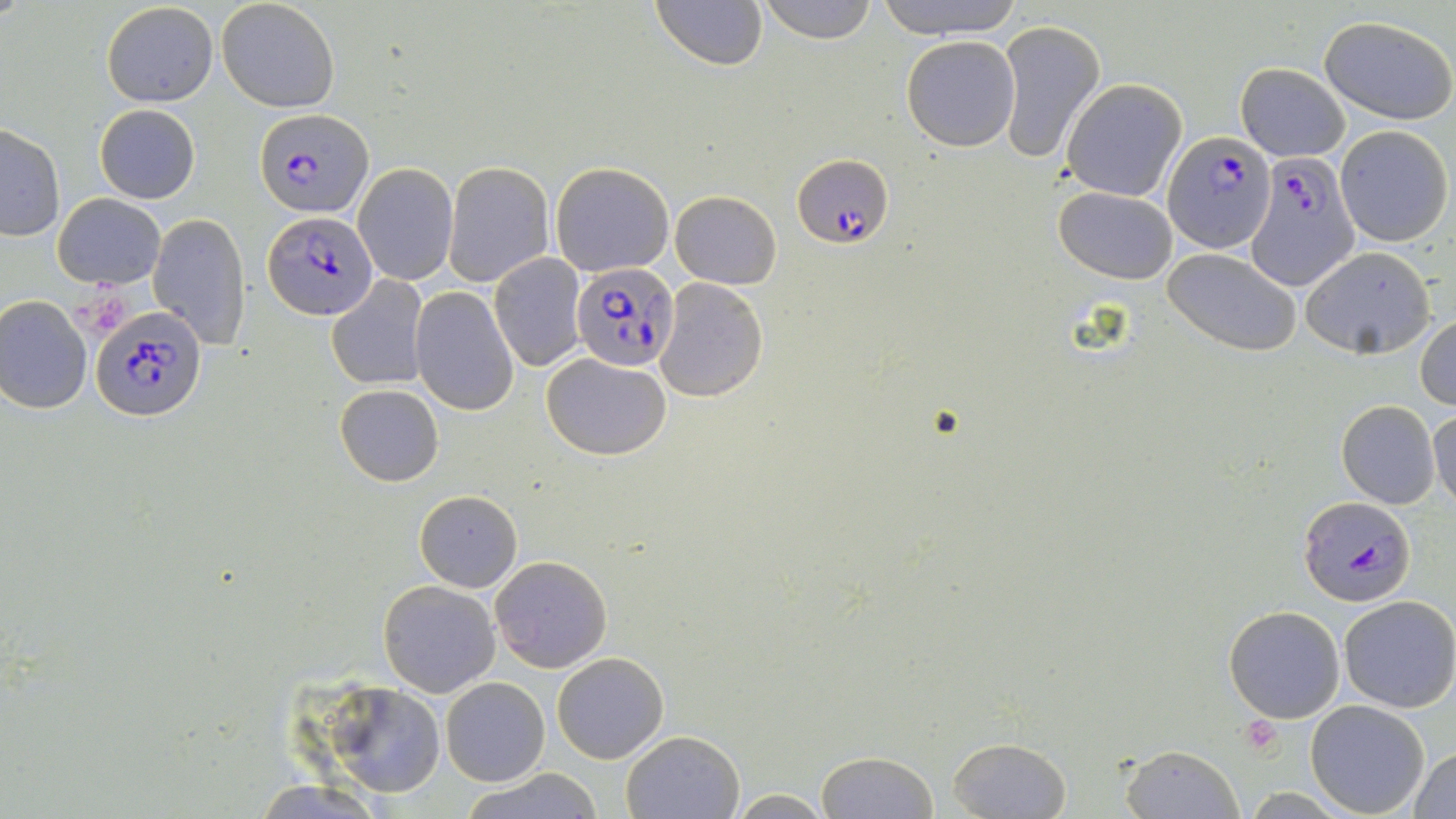

Approximate bounding boxes as (x1,y1)-(x2,y2) corner pairs in pixels. Plasmodium falciparum-infected red blood cell locations: (254,108)-(372,217), (1163,129)-(1276,250), (1246,151)-(1360,291), (793,152)-(895,249), (262,210)-(380,320), (570,262)-(680,369), (92,302)-(207,422), (1299,494)-(1414,605). Platelet locations: (1240,714)-(1285,757). Uninfected red blood cell locations: (217,0)-(340,112), (650,0)-(766,70), (756,0)-(877,44), (873,0)-(1026,39), (102,2)-(218,108), (1319,17)-(1455,123), (995,20)-(1106,165), (900,35)-(1020,152), (1234,63)-(1350,163), (1060,79)-(1187,202), (94,104)-(202,204), (0,125)-(65,240), (1334,125)-(1453,246), (443,162)-(554,287), (548,162)-(674,276), (352,163)-(458,286), (1053,186)-(1179,283), (670,190)-(782,289), (53,193)-(164,288), (147,213)-(250,349), (1300,246)-(1436,358), (1164,247)-(1302,354), (488,254)-(586,371), (326,275)-(429,391), (655,277)-(768,402), (411,287)-(520,415), (0,293)-(93,413), (1416,312)-(1456,411), (542,355)-(671,458), (334,383)-(443,487), (1336,399)-(1441,510), (1428,401)-(1456,514), (414,490)-(522,592), (491,555)-(612,672), (378,580)-(500,697), (1337,595)-(1456,713), (1224,604)-(1345,722), (552,652)-(668,763), (441,677)-(550,787), (316,682)-(449,800), (1304,700)-(1431,817), (620,730)-(744,818), (945,735)-(1072,818), (1118,744)-(1242,819), (1409,745)-(1456,818), (815,750)-(941,819), (461,768)-(605,819), (251,780)-(384,819), (726,790)-(837,817). Slide-level diagnosis: Plasmodium falciparum. Thin blood smear. Light microscopy. Captured at 1000x magnification. Image is 1456×819 pixels. One field of a larger specimen. May-Grünwald-Giemsa stain.